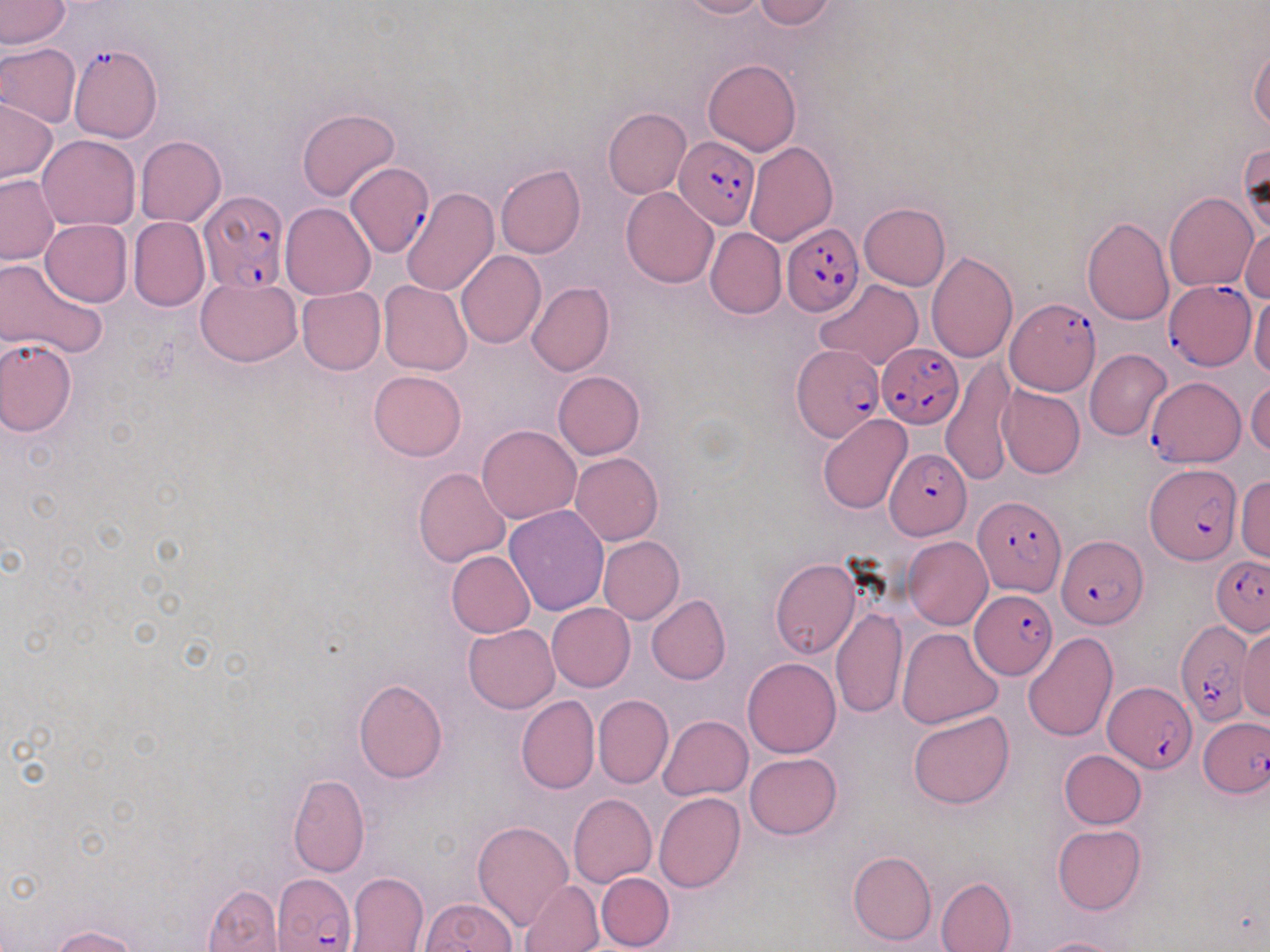
slide-level diagnosis = Plasmodium falciparum
magnification = 1000x
uninfected red blood cell locations (subset) = approximate bounding boxes as named x1/y1/x2/y2 corners in pixels: (x1=0, y1=0, x2=69, y2=49), (x1=676, y1=0, x2=768, y2=19), (x1=755, y1=0, x2=838, y2=29), (x1=1, y1=43, x2=81, y2=124), (x1=1248, y1=44, x2=1270, y2=133), (x1=703, y1=58, x2=801, y2=156), (x1=1, y1=97, x2=57, y2=184), (x1=296, y1=108, x2=400, y2=202), (x1=602, y1=108, x2=690, y2=198), (x1=38, y1=135, x2=140, y2=230), (x1=135, y1=137, x2=226, y2=226), (x1=744, y1=140, x2=837, y2=245), (x1=1239, y1=143, x2=1269, y2=239), (x1=496, y1=165, x2=585, y2=258), (x1=0, y1=175, x2=58, y2=264), (x1=621, y1=187, x2=719, y2=288), (x1=399, y1=188, x2=498, y2=297), (x1=1164, y1=193, x2=1257, y2=292), (x1=280, y1=202, x2=375, y2=300), (x1=858, y1=203, x2=951, y2=290), (x1=1081, y1=216, x2=1175, y2=326), (x1=128, y1=217, x2=209, y2=311), (x1=41, y1=219, x2=132, y2=307), (x1=1240, y1=225, x2=1269, y2=302), (x1=705, y1=227, x2=786, y2=319), (x1=456, y1=249, x2=546, y2=349), (x1=925, y1=251, x2=1019, y2=364), (x1=0, y1=260, x2=106, y2=359), (x1=196, y1=277, x2=302, y2=366), (x1=378, y1=279, x2=471, y2=375), (x1=815, y1=279, x2=921, y2=368), (x1=527, y1=282, x2=614, y2=376), (x1=296, y1=286, x2=385, y2=375), (x1=1248, y1=291, x2=1270, y2=377), (x1=0, y1=337, x2=77, y2=437), (x1=1084, y1=349, x2=1172, y2=440), (x1=370, y1=371, x2=465, y2=461), (x1=553, y1=371, x2=645, y2=460), (x1=1246, y1=380, x2=1270, y2=456), (x1=997, y1=386, x2=1085, y2=479), (x1=818, y1=414, x2=912, y2=514), (x1=477, y1=424, x2=580, y2=523), (x1=570, y1=452, x2=663, y2=546), (x1=414, y1=468, x2=510, y2=567), (x1=1235, y1=477, x2=1270, y2=563), (x1=504, y1=505, x2=611, y2=616), (x1=904, y1=535, x2=993, y2=630), (x1=598, y1=536, x2=683, y2=624), (x1=446, y1=550, x2=536, y2=637), (x1=771, y1=559, x2=861, y2=658), (x1=647, y1=594, x2=730, y2=686), (x1=546, y1=602, x2=635, y2=692), (x1=831, y1=607, x2=906, y2=718), (x1=463, y1=624, x2=559, y2=714), (x1=1237, y1=626, x2=1270, y2=722), (x1=896, y1=628, x2=1002, y2=729), (x1=1023, y1=632, x2=1119, y2=743), (x1=742, y1=658, x2=840, y2=758), (x1=353, y1=678, x2=447, y2=784), (x1=593, y1=694, x2=673, y2=789), (x1=516, y1=695, x2=600, y2=794), (x1=907, y1=710, x2=1015, y2=808), (x1=659, y1=715, x2=753, y2=800), (x1=1058, y1=749, x2=1146, y2=829), (x1=745, y1=753, x2=841, y2=839), (x1=288, y1=773, x2=369, y2=876), (x1=654, y1=792, x2=745, y2=892), (x1=568, y1=793, x2=656, y2=888), (x1=472, y1=820, x2=574, y2=929), (x1=1052, y1=823, x2=1145, y2=914), (x1=847, y1=851, x2=936, y2=946), (x1=345, y1=872, x2=428, y2=951), (x1=596, y1=872, x2=674, y2=951), (x1=935, y1=876, x2=1017, y2=952), (x1=520, y1=880, x2=604, y2=951), (x1=202, y1=884, x2=283, y2=952), (x1=420, y1=898, x2=517, y2=951), (x1=51, y1=926, x2=140, y2=952), (x1=1034, y1=936, x2=1130, y2=952)
image size = 1270×952 pixels
field of view = one of a larger specimen
preparation = thin blood film
Plasmodium falciparum-infected red blood cell locations (subset) = approximate bounding boxes as named x1/y1/x2/y2 corners in pixels: (x1=69, y1=42, x2=161, y2=143), (x1=675, y1=135, x2=761, y2=229), (x1=345, y1=162, x2=433, y2=257), (x1=198, y1=189, x2=290, y2=296), (x1=782, y1=224, x2=864, y2=317), (x1=1164, y1=281, x2=1256, y2=372), (x1=1006, y1=298, x2=1101, y2=396), (x1=876, y1=341, x2=963, y2=430), (x1=790, y1=345, x2=884, y2=442), (x1=1147, y1=378, x2=1243, y2=467), (x1=884, y1=449, x2=970, y2=540), (x1=1146, y1=464, x2=1240, y2=564), (x1=973, y1=496, x2=1065, y2=597), (x1=1056, y1=537, x2=1145, y2=631), (x1=1210, y1=556, x2=1270, y2=635), (x1=970, y1=590, x2=1057, y2=680), (x1=1175, y1=621, x2=1251, y2=728), (x1=1103, y1=681, x2=1197, y2=773), (x1=1199, y1=714, x2=1268, y2=795), (x1=272, y1=872, x2=355, y2=949)
modality = optical microscopy
stain = May-Grünwald-Giemsa